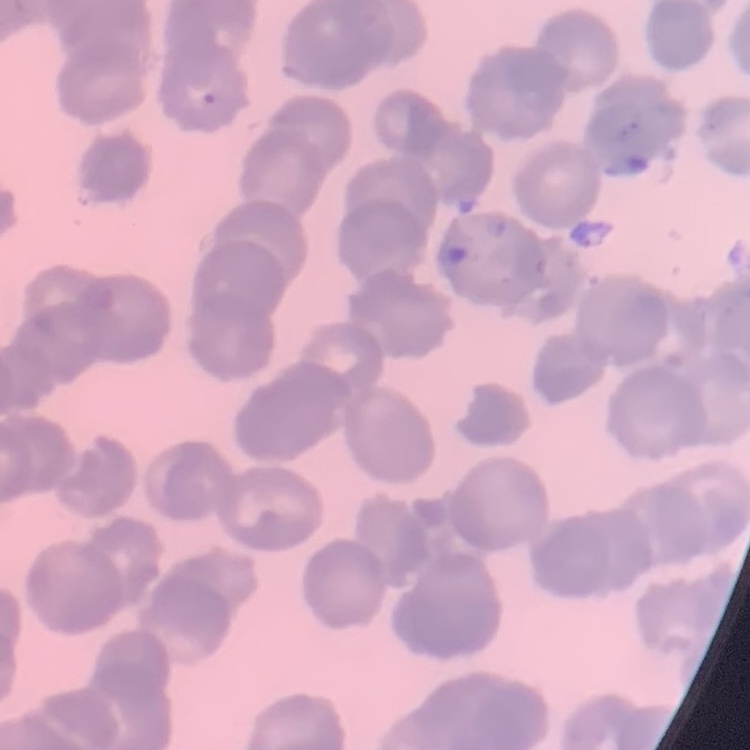
Summary:
  - Erythrocyte morphology: rouleaux formation
  - Image type: one tile cut from a larger photomicrograph
  - Stain: Field's or Giemsa
  - Preparation: thin peripheral smear